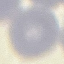
Result: negative for malaria parasites. Cell patch, automatically extracted from a larger field of view and resized to 64 × 64 pixels. Giemsa-stained preparation. Photographed with a smartphone camera at the microscope eyepiece. Thin blood smear.